Identify the cell.
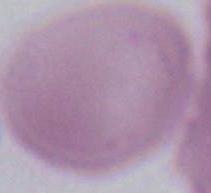

This is an erythrocyte.

modality = photomicrograph
magnification = 1000x